Identify the parasite.
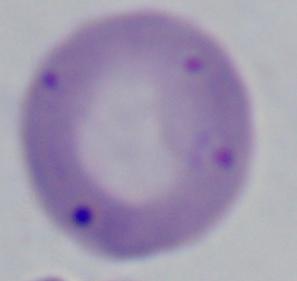
This is Babesia.

Summary:
  - Magnification: 1000x
  - Modality: micrograph